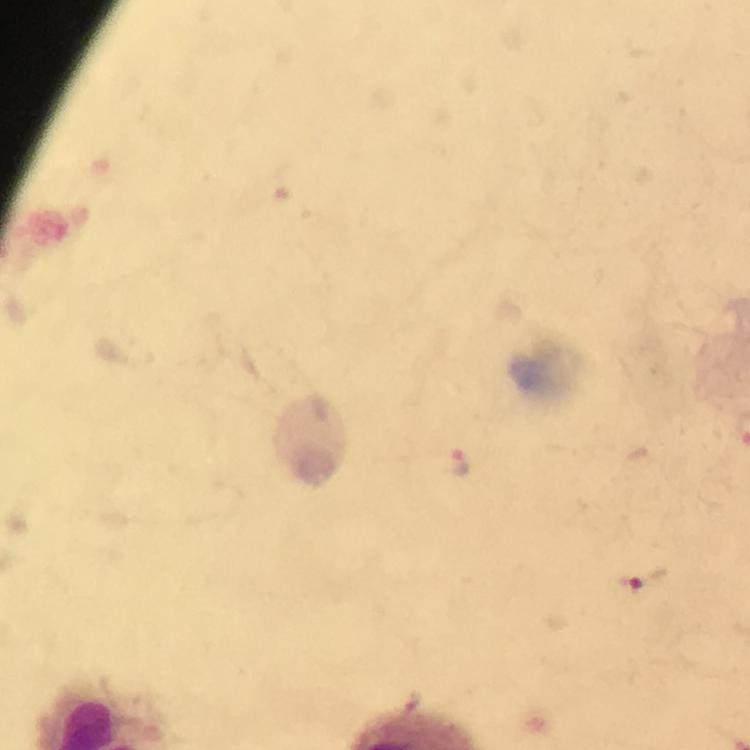 Approximate centers as {x, y} in pixels. Malaria parasite locations: {459, 463}, {641, 581}. Image is 750×750 pixels. A crop from one field of view. Immersion oil applied. 100x magnification. Thick smear. Photographed with a smartphone mounted on the microscope. Giemsa-stained preparation. From a malaria diagnostic workup.